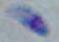

Summary:
  - Modality: micrograph
  - Magnification: 1000x
  - Identification: Toxoplasma gondii